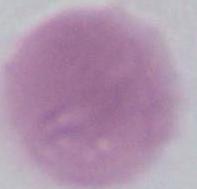
Captured at 1000x magnification. Micrograph. A red blood cell is shown.